Locate every blood parasite and identify its species.
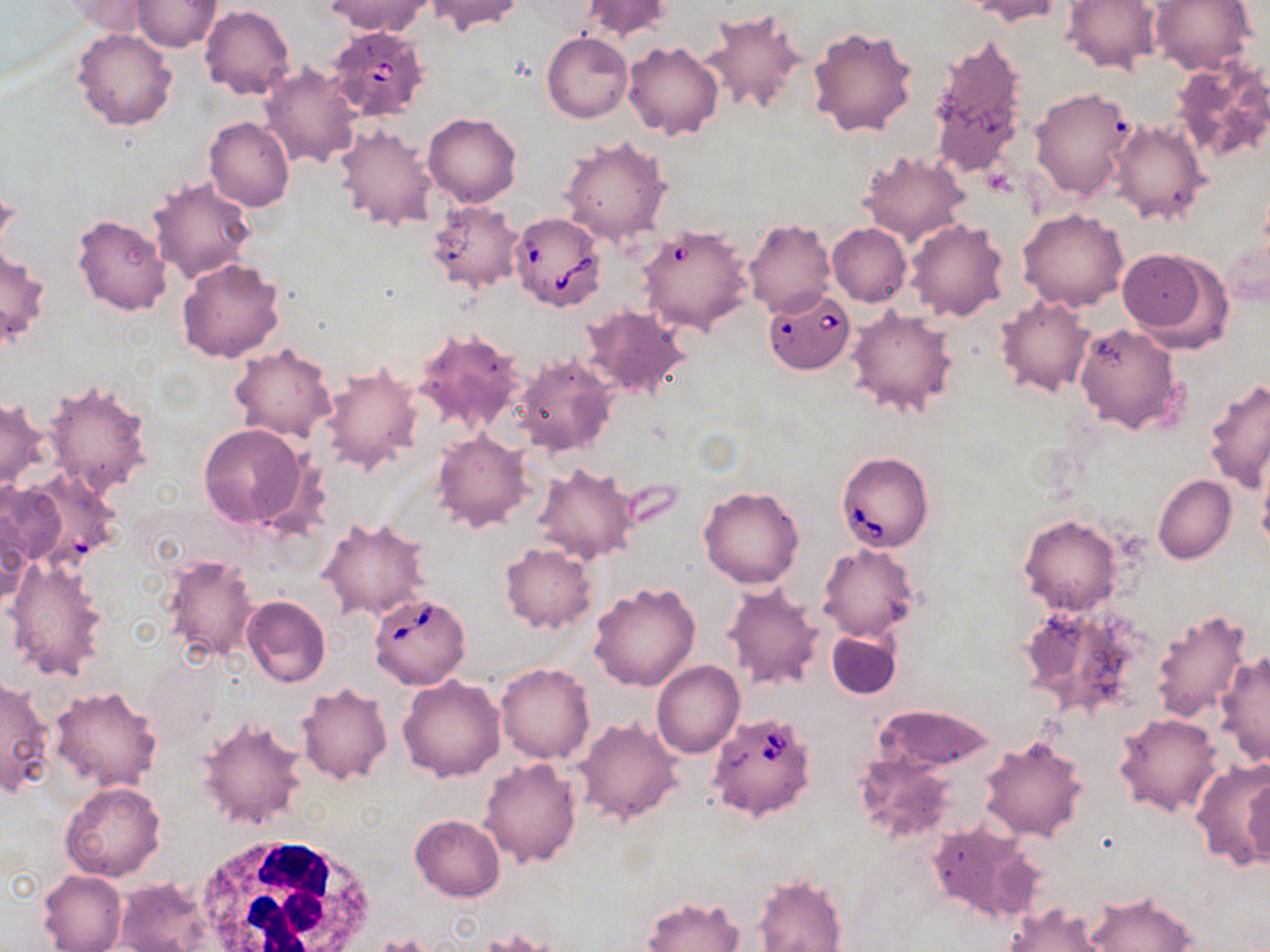

Approximate bounding boxes as (x1, y1, x2, y2) in pixels.
Babesia divergens-infected red blood cells: (326, 21, 433, 118), (510, 212, 606, 311), (636, 222, 753, 339), (762, 289, 855, 375), (836, 452, 934, 553), (367, 592, 471, 689), (708, 711, 816, 822).
No Plasmodium falciparum, Plasmodium ovale, Plasmodium malariae, Plasmodium vivax, or Trypanosoma brucei observed.

Summary:
  - Uninfected red blood cell locations: (327, 0, 431, 37), (424, 0, 522, 36), (581, 0, 671, 43), (1061, 0, 1160, 74), (1149, 0, 1255, 76), (59, 1, 152, 36), (131, 1, 222, 52), (966, 1, 1065, 27), (200, 5, 295, 100), (699, 10, 808, 117), (807, 26, 919, 139), (72, 28, 178, 131), (542, 32, 633, 122), (925, 32, 1026, 177), (623, 41, 724, 141), (1170, 57, 1270, 167), (260, 62, 363, 169), (1030, 86, 1136, 201), (422, 113, 522, 207), (205, 117, 294, 211), (1107, 117, 1209, 224), (334, 123, 441, 233), (559, 135, 673, 247), (856, 148, 970, 245), (147, 177, 256, 284), (0, 190, 18, 262), (426, 201, 526, 294), (1018, 207, 1129, 311), (72, 214, 172, 316), (743, 218, 834, 318), (905, 218, 1009, 322), (827, 224, 911, 306), (1115, 247, 1232, 349), (1, 248, 51, 349), (176, 259, 285, 364), (1087, 261, 1210, 414), (993, 293, 1095, 397), (583, 305, 692, 403), (847, 305, 958, 417), (1073, 323, 1185, 436), (414, 328, 526, 436), (229, 344, 337, 442), (513, 351, 618, 457), (319, 364, 421, 473), (41, 378, 155, 497), (1204, 378, 1270, 492), (0, 397, 49, 490), (198, 422, 313, 531), (431, 431, 532, 532), (1257, 450, 1270, 557), (532, 463, 638, 565), (1153, 475, 1236, 564), (0, 477, 74, 565), (700, 485, 804, 588), (1, 503, 34, 606), (318, 515, 432, 621), (1019, 515, 1122, 615), (499, 542, 595, 632), (820, 544, 919, 642), (163, 554, 261, 663), (4, 559, 110, 680), (588, 581, 700, 691), (722, 582, 825, 691), (242, 595, 330, 688), (1020, 600, 1151, 723), (1149, 607, 1252, 723), (826, 627, 902, 700), (376, 628, 486, 760), (1214, 651, 1269, 767), (144, 656, 223, 748), (653, 661, 744, 758), (496, 663, 593, 763), (397, 674, 506, 780), (0, 678, 54, 798), (296, 683, 393, 785), (51, 686, 163, 792), (877, 704, 994, 773), (1114, 712, 1222, 817), (197, 716, 308, 829), (572, 716, 684, 824), (979, 736, 1087, 841), (854, 755, 957, 845), (479, 757, 582, 868), (1190, 757, 1270, 869), (1242, 770, 1269, 871), (61, 782, 167, 882), (410, 814, 505, 900), (926, 821, 1043, 924), (39, 870, 127, 952), (753, 873, 848, 952), (114, 877, 212, 952), (1081, 891, 1198, 951), (642, 896, 744, 952), (1001, 902, 1113, 952), (371, 935, 438, 952)
  - White blood cell locations: (188, 831, 374, 952)
  - Slide-level diagnosis: Babesia divergens
  - Stain: May-Grünwald-Giemsa
  - Modality: light microscopy
  - Magnification: 1000x
  - Image size: 1270×952 pixels
  - Field of view: one of a larger specimen
  - Preparation: thin blood smear